Name the parasite shown.
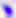

This is Toxoplasma gondii.

magnification = 400x
modality = photomicrograph